Outline each uninfected red blood cell.
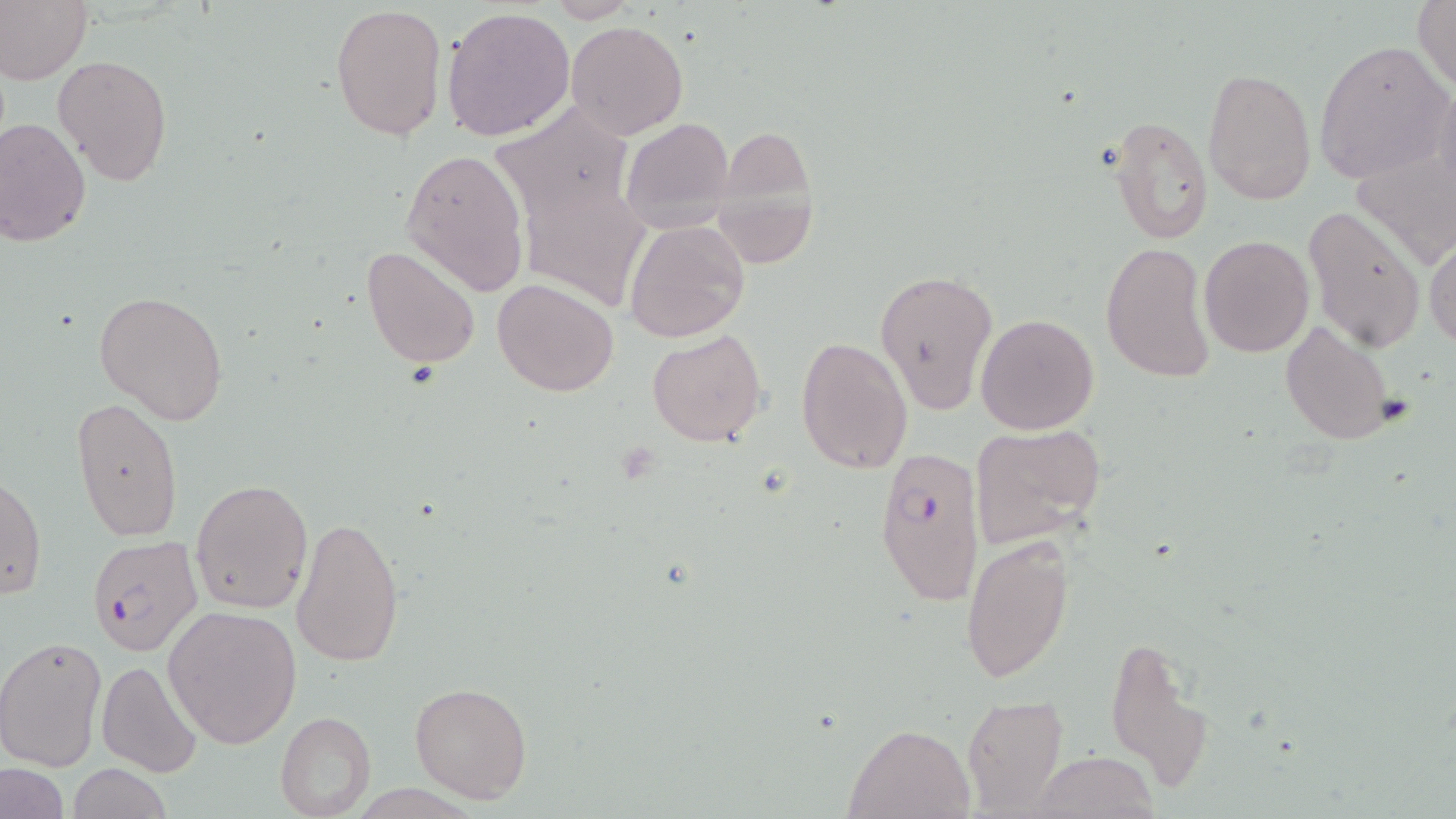
Approximate bounding boxes as (x1,y1)-(x2,y2) corner pairs in pixels.
Uninfected red blood cells: (1413,0)-(1456,93), (542,1)-(643,23), (0,2)-(91,82), (330,2)-(447,140), (441,6)-(576,142), (566,19)-(689,138), (1314,39)-(1453,185), (53,55)-(172,185), (1202,67)-(1316,204), (1108,113)-(1215,246), (620,117)-(734,230), (0,118)-(92,247), (711,129)-(820,269), (1351,142)-(1455,270), (401,148)-(531,296), (523,176)-(652,312), (1304,205)-(1427,352), (623,220)-(750,343), (1199,235)-(1315,358), (1426,238)-(1456,350), (1101,242)-(1215,383), (361,245)-(482,369), (873,268)-(1000,414), (493,278)-(619,398), (94,290)-(229,424), (975,313)-(1099,435), (1280,320)-(1398,446), (648,327)-(766,447), (794,334)-(913,475), (72,397)-(183,543), (968,423)-(1104,551), (1,473)-(45,602), (189,478)-(313,615), (289,514)-(405,669), (959,532)-(1076,684), (162,605)-(302,748), (1105,633)-(1211,788), (0,636)-(107,770), (96,659)-(203,777), (408,681)-(533,804), (962,694)-(1068,816), (274,711)-(375,817), (845,724)-(972,818), (1030,751)-(1159,819), (66,763)-(173,818), (2,765)-(68,818).

Plasmodium falciparum-infected red blood cell locations = approximate bounding boxes as (x1,y1)-(x2,y2) corner pairs in pixels: (875,450)-(986,605), (85,535)-(203,659)
slide-level diagnosis = Plasmodium falciparum
stain = May-Grünwald-Giemsa
magnification = 1000x
field of view = single
modality = optical microscopy
preparation = thin blood film
image size = 1456×819 pixels